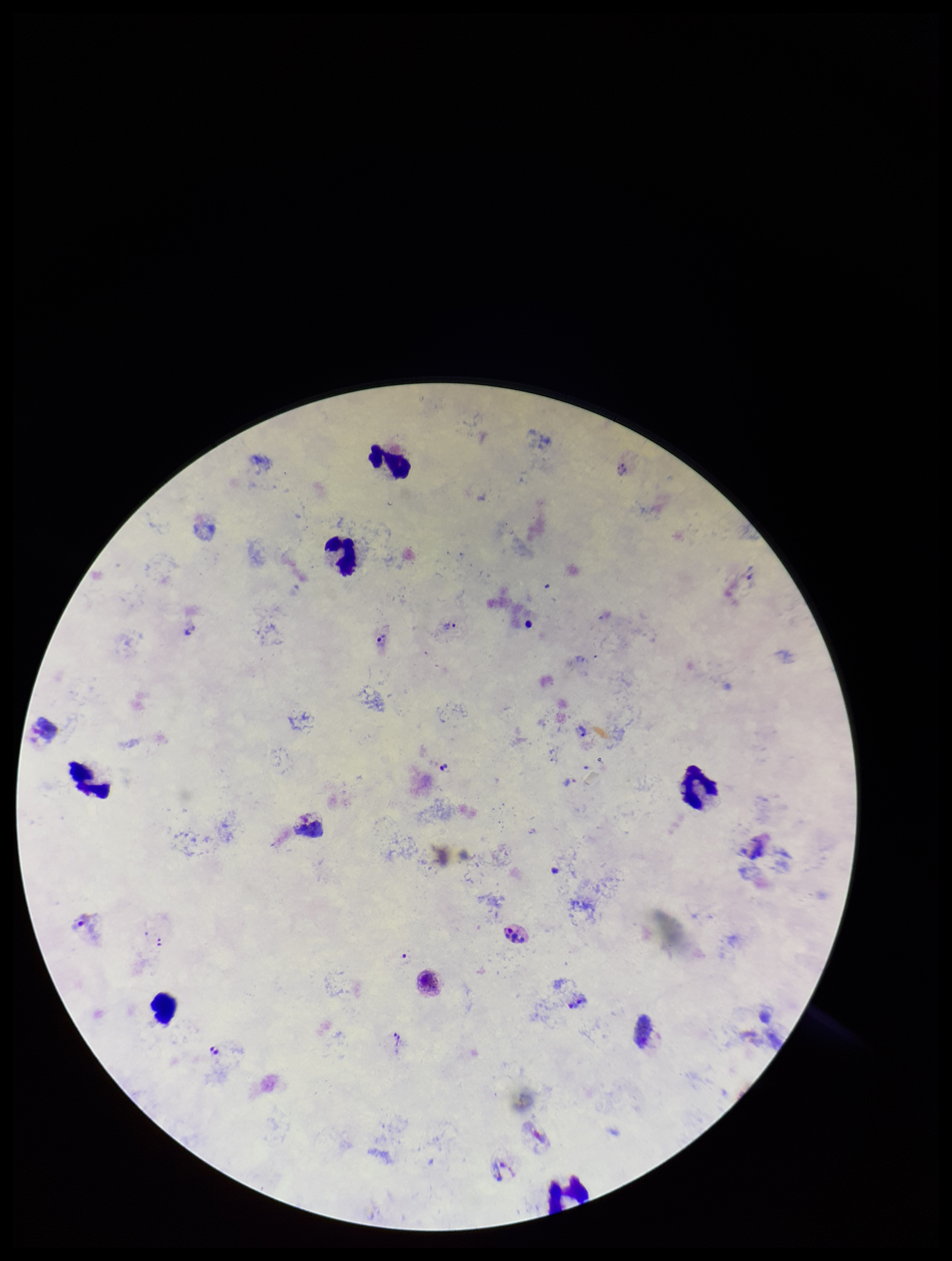
Single field of view. Preparation: thick smear. Smartphone photograph taken through the eyepiece of a microscope. Plasmodium parasites: identified. Species reported for this patient: Plasmodium vivax. Image is 952×1261 pixels. Stained with Giemsa. Leukocyte count: 6. Parasite count: 8. Patient malaria status: infected.